Assess for Plasmodium parasites.
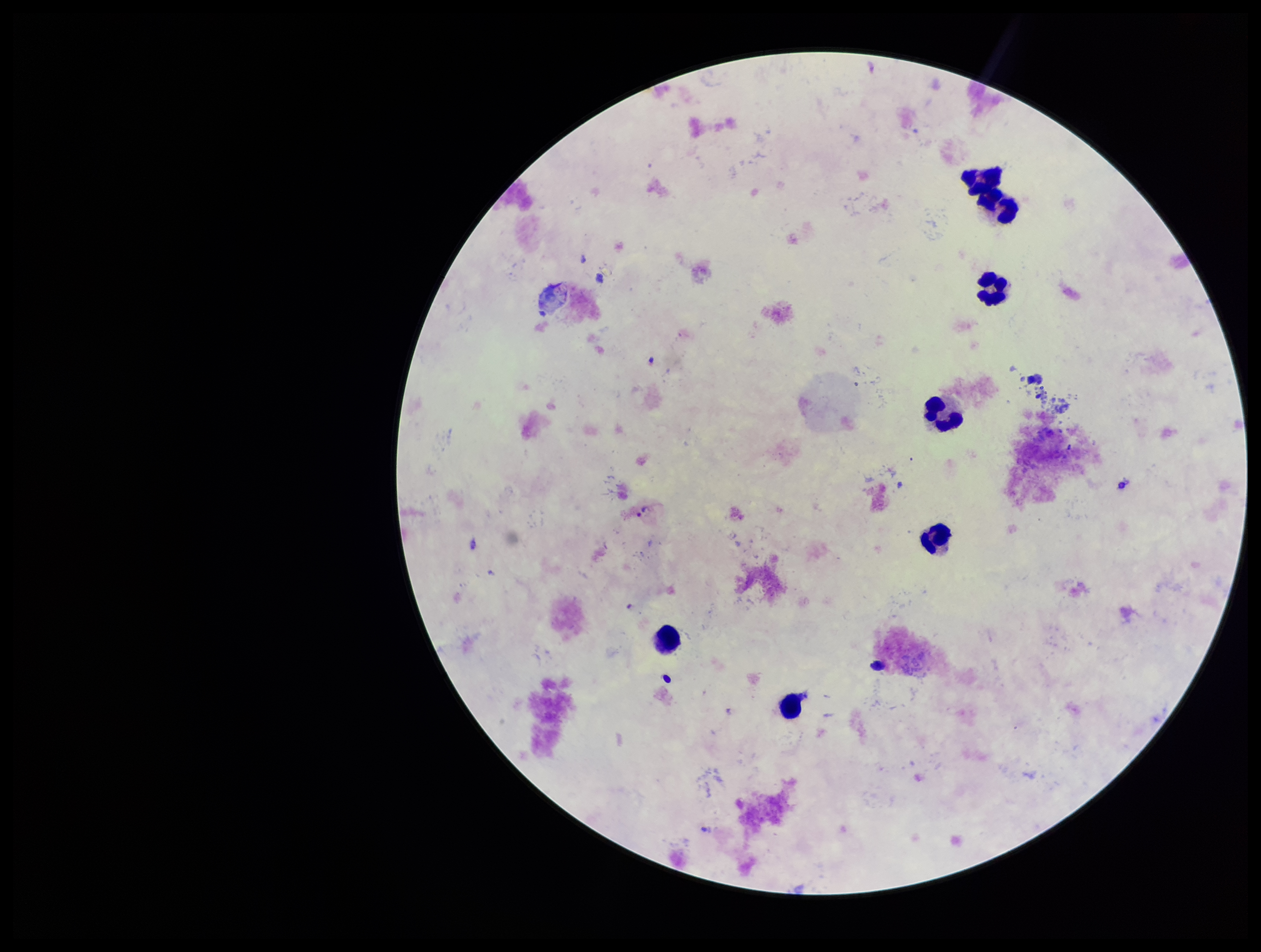
Identified.

Summary:
  - Stain: Giemsa
  - Preparation: thick
  - Patient malaria status: positive
  - Field of view: single
  - Parasite count: 2
  - Capture: smartphone photograph through the microscope eyepiece
  - Leukocyte count: 7
  - Species reported for this patient: Plasmodium vivax
  - Image size: 1261×952 pixels